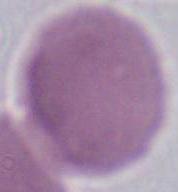

Summary:
  - Magnification: 1000x
  - Identification: erythrocyte
  - Modality: photomicrograph